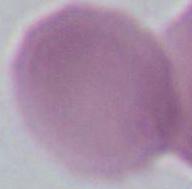
1000x magnification. A red blood cell is shown. Micrograph.